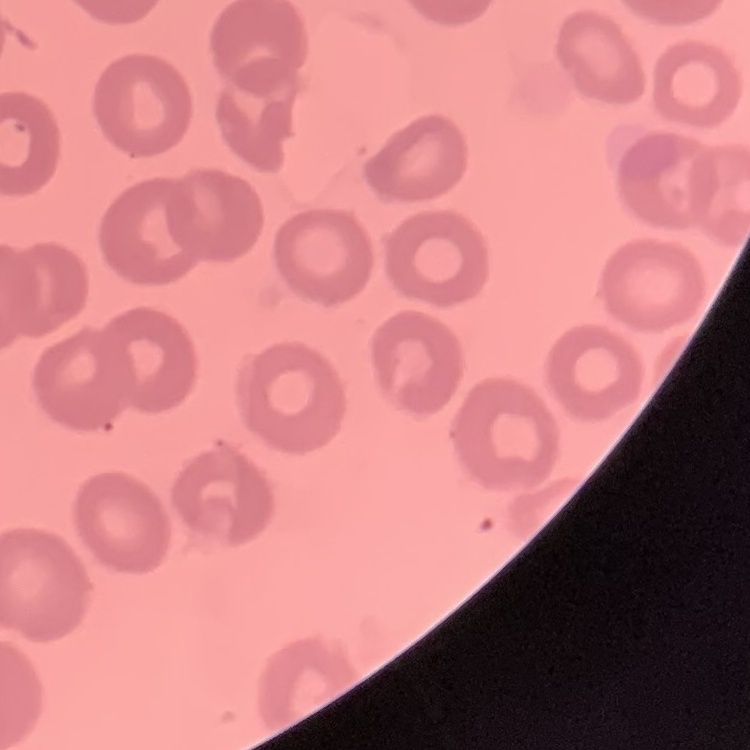 The erythrocytes show no rouleaux formation. Field's or Giemsa stain. Square crop of a larger photomicrograph. Thin blood smear.